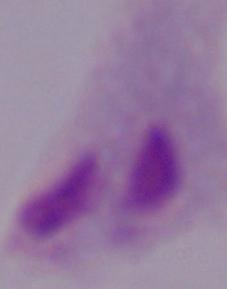

modality = micrograph
magnification = 1000x
identification = trichomonad